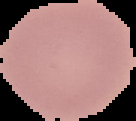
Summary:
  - Image size: 136×121 pixels
  - Image type: cell region segmented out of the field of view; surrounding area masked to black
  - Preparation: thin blood film
  - Malaria status: uninfected